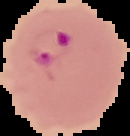

result = Plasmodium parasites identified
image size = 130×136 pixels
preparation = thin blood film
image type = cell region segmented out of the field of view; surrounding area masked to black